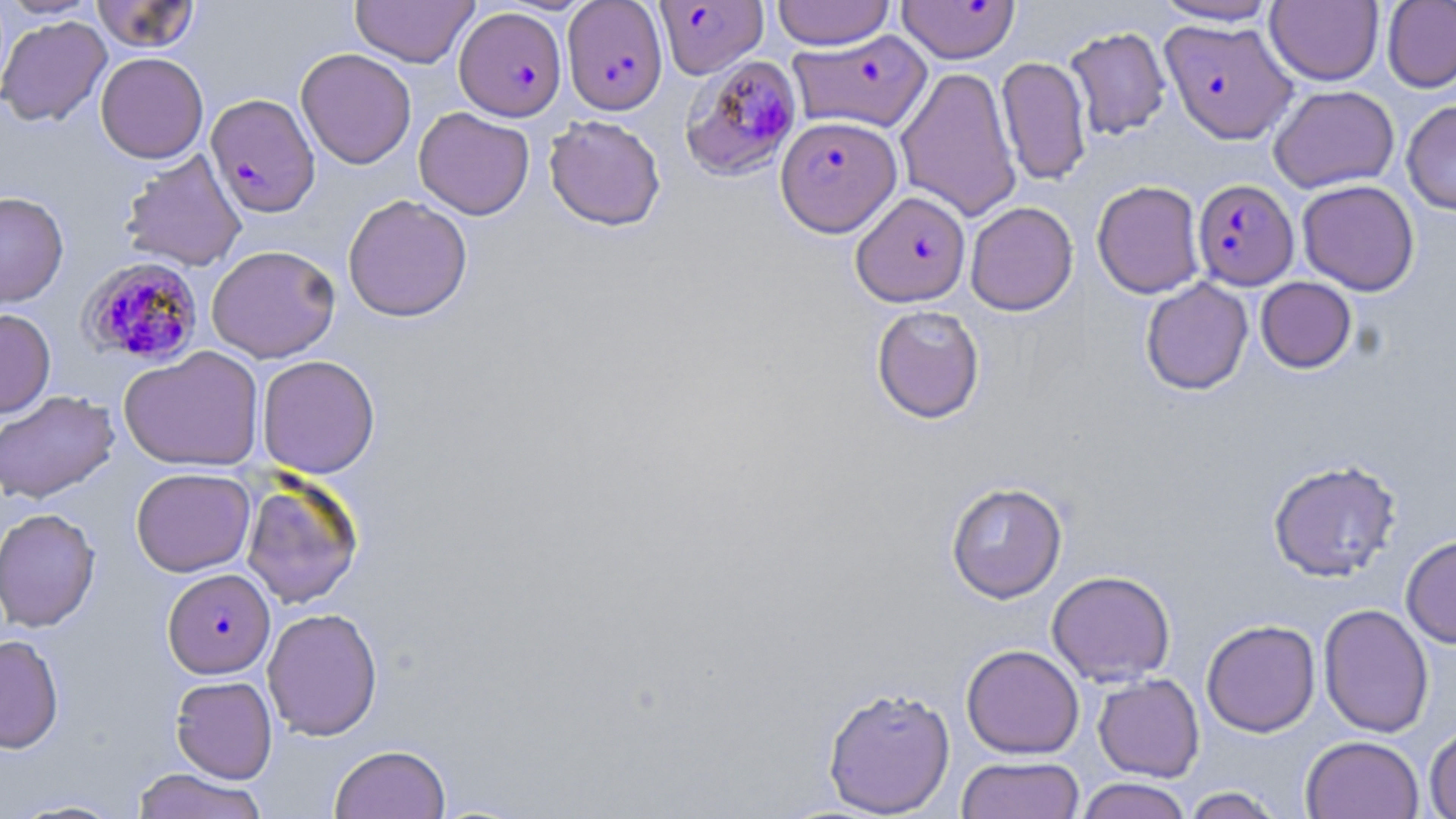
Approximate bounding boxes as [x1, y1, x2, y2] in pixels. Plasmodium falciparum-infected red blood cell locations: [895, 0, 1020, 63], [562, 1, 668, 115], [655, 1, 767, 78], [454, 7, 566, 121], [1160, 18, 1297, 144], [788, 30, 933, 133], [678, 50, 798, 179], [205, 93, 320, 218], [776, 115, 901, 236], [1192, 179, 1299, 289], [852, 191, 971, 307], [79, 257, 204, 367], [162, 568, 275, 678]. Uninfected red blood cell locations: [1, 0, 102, 19], [350, 0, 478, 67], [772, 0, 894, 50], [1151, 0, 1282, 26], [1266, 0, 1383, 85], [91, 1, 201, 53], [1382, 1, 1456, 93], [0, 15, 112, 127], [1064, 26, 1171, 140], [295, 48, 417, 169], [95, 52, 208, 163], [996, 56, 1092, 186], [895, 66, 1022, 222], [1268, 85, 1399, 193], [1401, 99, 1456, 215], [414, 107, 535, 220], [543, 114, 666, 231], [119, 149, 248, 272], [1092, 180, 1205, 299], [1297, 180, 1420, 296], [0, 191, 69, 309], [342, 194, 473, 322], [965, 201, 1078, 316], [206, 244, 340, 363], [1256, 277, 1356, 373], [1140, 278, 1253, 395], [871, 305, 985, 424], [0, 309, 56, 418], [118, 346, 264, 472], [257, 355, 380, 479], [0, 390, 119, 504], [1267, 459, 1403, 582], [130, 467, 255, 577], [241, 477, 364, 609], [945, 482, 1068, 603], [0, 507, 101, 632], [1400, 533, 1456, 648], [1047, 570, 1176, 686], [1318, 603, 1434, 738], [262, 607, 383, 741], [1201, 619, 1321, 737], [0, 634, 64, 754], [961, 644, 1084, 758], [1093, 673, 1205, 782], [170, 675, 278, 783], [822, 685, 956, 817], [1424, 724, 1456, 819], [1300, 735, 1424, 818], [330, 743, 451, 819], [956, 756, 1085, 819], [131, 768, 268, 819], [1075, 778, 1194, 819], [1181, 786, 1286, 819], [7, 797, 129, 818]. Slide-level diagnosis: Plasmodium falciparum. Thin blood smear. May-Grünwald-Giemsa-stained preparation. Optical microscopy. Image is 1456×819 pixels. Single field of view. 1000x magnification.